Locate and identify every blood parasite.
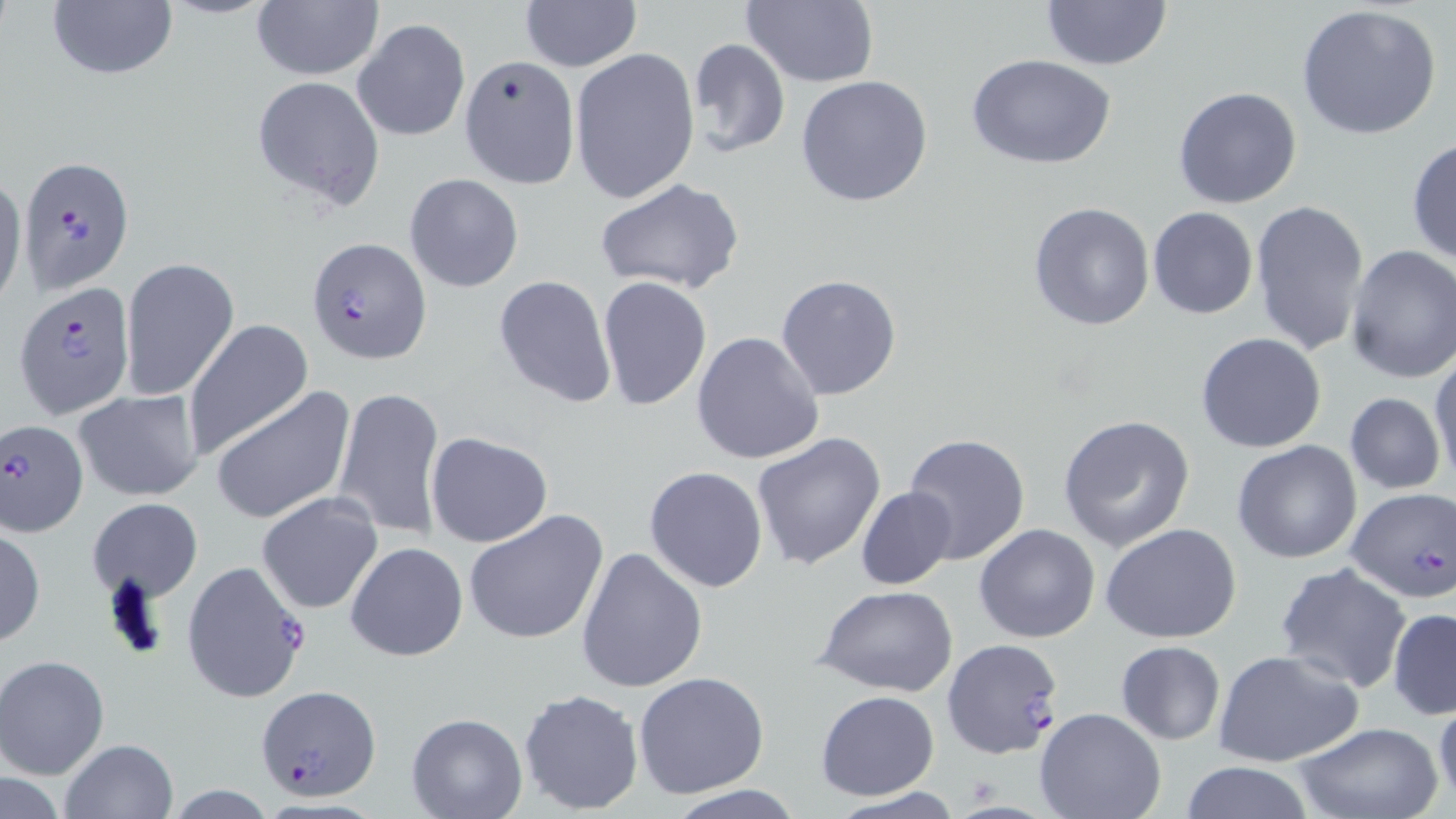

Approximate bounding boxes as [x1, y1, x2, y2] in pixels.
Plasmodium falciparum-infected red blood cells: [17, 156, 134, 293], [305, 235, 433, 366], [12, 281, 137, 421], [2, 418, 90, 536], [1344, 488, 1454, 603], [180, 560, 311, 704], [253, 686, 381, 801].
No Plasmodium ovale, Plasmodium malariae, Plasmodium vivax, Babesia divergens, or Trypanosoma brucei observed.

slide-level diagnosis = Plasmodium falciparum
field of view = one of a larger specimen
stain = May-Grünwald-Giemsa
modality = light microscopy
image size = 1456×819 pixels
magnification = 1000x
preparation = thin blood film
uninfected red blood cell locations = approximate bounding boxes as [x1, y1, x2, y2] in pixels: [47, 0, 178, 83], [742, 0, 879, 88], [518, 1, 642, 72], [1039, 1, 1174, 72], [251, 2, 382, 81], [1296, 3, 1444, 143], [353, 18, 470, 142], [685, 37, 791, 157], [569, 47, 699, 204], [457, 55, 580, 190], [968, 55, 1116, 170], [251, 76, 387, 209], [795, 77, 934, 207], [1172, 86, 1303, 210], [1407, 138, 1456, 265], [0, 172, 26, 315], [405, 173, 524, 292], [598, 179, 744, 296], [1250, 197, 1370, 357], [1027, 201, 1156, 333], [1147, 206, 1258, 320], [1342, 244, 1456, 383], [120, 257, 239, 402], [776, 274, 901, 399], [493, 275, 616, 410], [597, 275, 711, 412], [184, 321, 314, 461], [692, 331, 825, 466], [1195, 332, 1327, 454], [1430, 351, 1456, 486], [212, 385, 356, 526], [332, 385, 445, 540], [73, 390, 204, 501], [1343, 393, 1446, 493], [1059, 415, 1195, 551], [426, 430, 553, 547], [751, 431, 886, 572], [903, 432, 1031, 566], [1231, 440, 1363, 564], [644, 465, 767, 593], [855, 486, 955, 590], [256, 492, 383, 615], [86, 497, 203, 603], [465, 510, 609, 648], [0, 524, 45, 648], [974, 524, 1101, 644], [1101, 524, 1243, 644], [345, 541, 469, 663], [576, 546, 709, 692], [1276, 561, 1410, 691], [817, 585, 957, 697], [1388, 608, 1456, 719], [942, 638, 1066, 758], [1116, 640, 1226, 744], [1213, 648, 1364, 767], [0, 654, 111, 780], [632, 672, 771, 798], [517, 687, 644, 815], [816, 690, 940, 801], [1433, 694, 1455, 807], [1034, 708, 1166, 819], [405, 713, 527, 819], [1291, 721, 1446, 819], [59, 738, 180, 819], [1177, 761, 1315, 818], [1, 773, 66, 818], [157, 782, 281, 818], [667, 786, 804, 818]